Point out each Plasmodium parasite and each leukocyte.
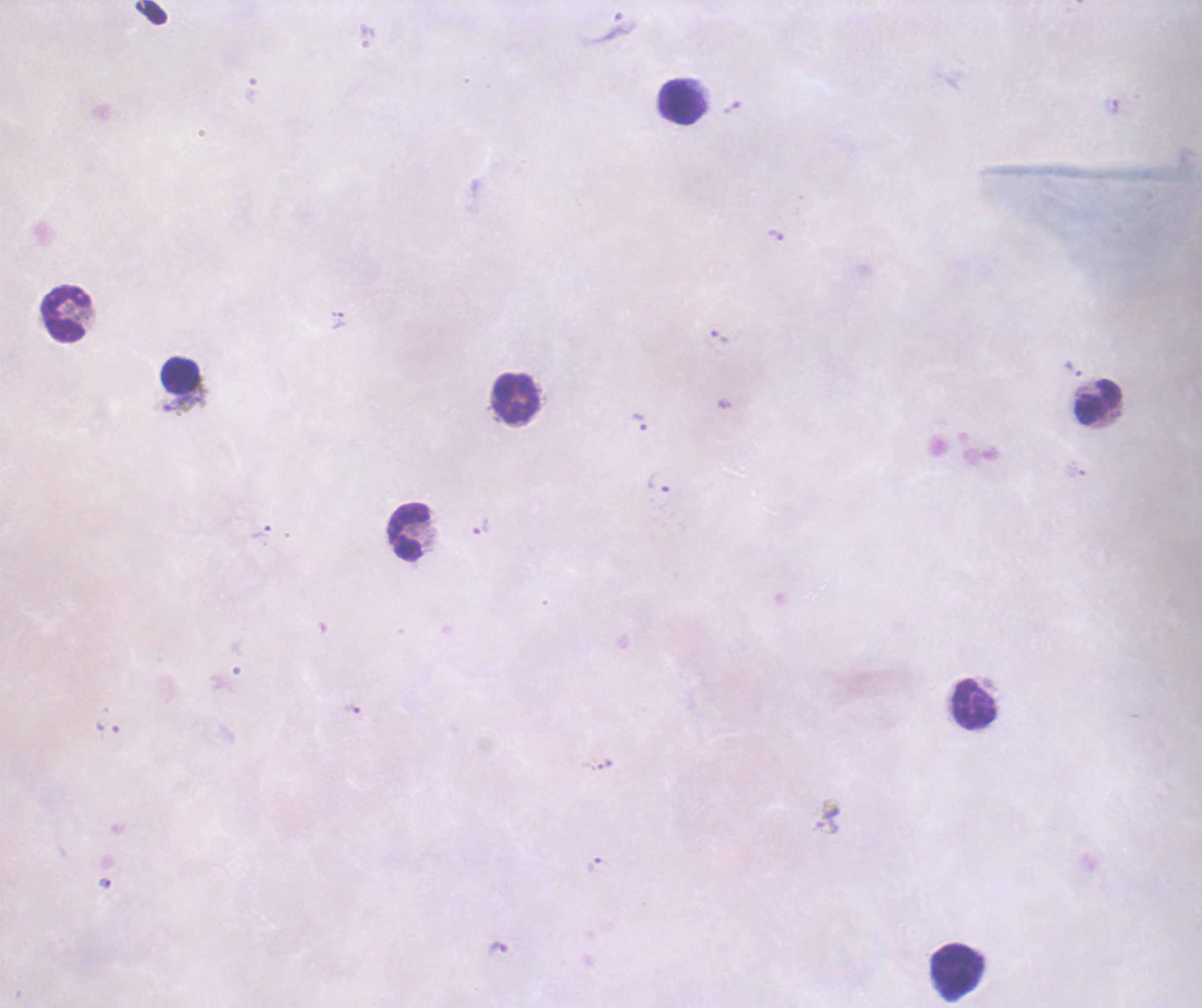

Approximate centers as (x, y) in pixels.
Trophozoites: (614, 29), (776, 235), (339, 321), (1073, 369), (184, 403), (639, 422), (659, 483), (481, 527), (262, 532), (352, 709), (595, 865), (104, 884), (498, 948).
Gametocytes: (828, 817).
No schizont forms observed.
Leukocytes: (683, 103), (65, 316), (180, 374), (517, 399), (1098, 402), (409, 531), (973, 705), (958, 972).

Previously used in a real diagnosis. Image is 1202×1008 pixels. Single field of view. Background quality: poor. Coloration quality: bad. Thick smear of blood. Romanowsky stain. 100x magnification.